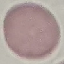

Result: no malaria parasites seen. Automatically extracted cell patch, resized to 64 × 64 pixels. Acquired by smartphone through the microscope eyepiece. Giemsa-stained preparation. Thin smear of blood.